Name the blood parasite species.
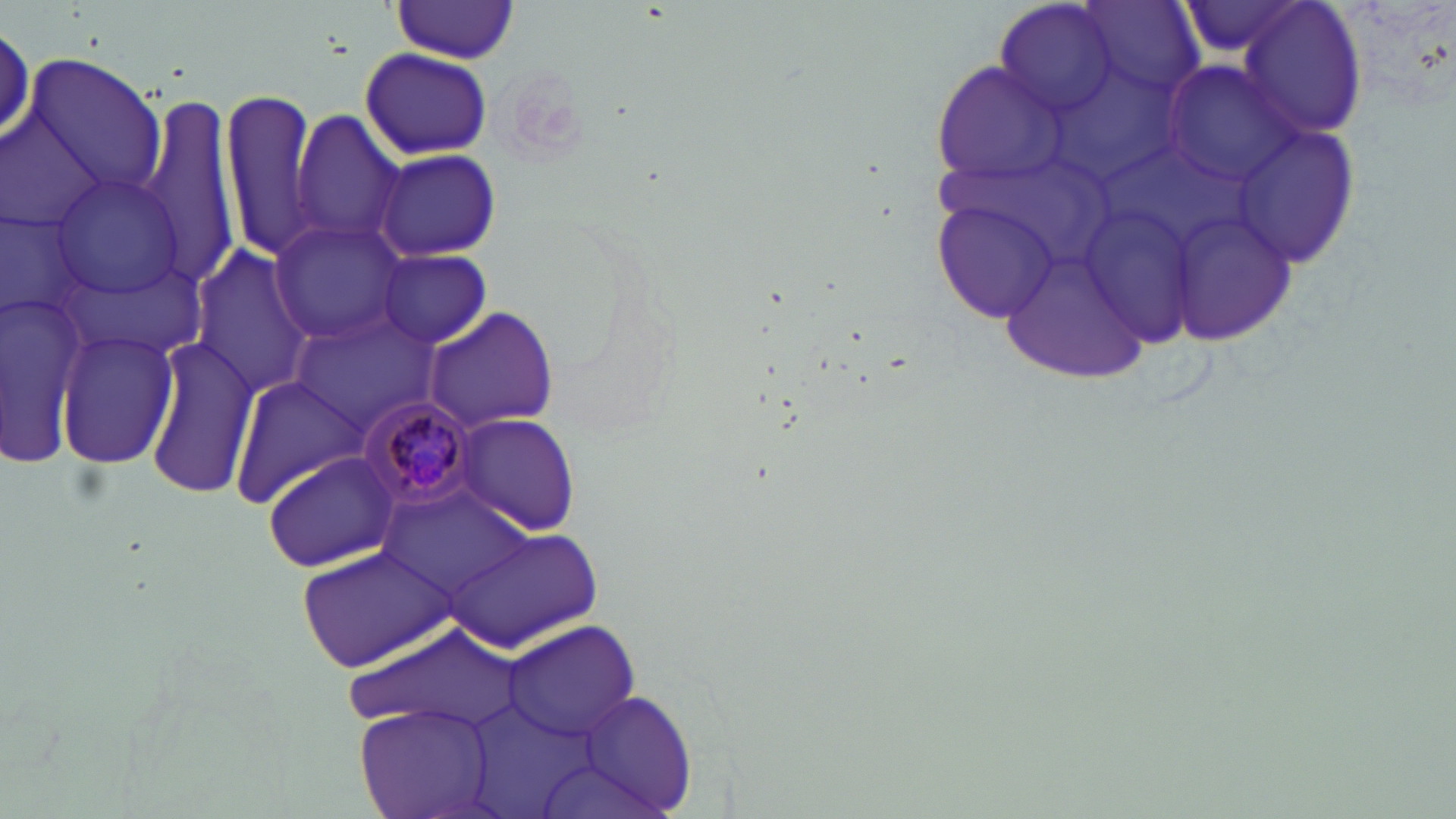

Plasmodium malariae.

Approximate bounding boxes as (x1, y1, x2, y2) in pixels. Uninfected red blood cell locations: (991, 0, 1121, 119), (1076, 1, 1203, 98), (1174, 1, 1319, 62), (387, 2, 521, 63), (1238, 2, 1367, 140), (360, 48, 492, 160), (22, 53, 165, 201), (933, 61, 1060, 188), (1160, 62, 1300, 187), (129, 90, 244, 291), (220, 90, 325, 262), (291, 109, 407, 251), (1232, 127, 1361, 268), (373, 147, 502, 261), (51, 173, 191, 298), (933, 200, 1061, 323), (1170, 206, 1302, 344), (269, 219, 409, 342), (999, 234, 1155, 388), (189, 243, 316, 399), (376, 250, 493, 347), (1, 282, 98, 465), (422, 305, 561, 431), (296, 313, 440, 424), (56, 329, 180, 471), (144, 338, 260, 499), (228, 373, 370, 508), (453, 414, 583, 535), (262, 450, 404, 573), (379, 485, 535, 605), (448, 524, 605, 651), (298, 545, 457, 671), (502, 620, 642, 744), (349, 623, 531, 734), (568, 690, 697, 812), (356, 703, 496, 819). Plasmodium malariae-infected red blood cell locations: (356, 397, 478, 516). Optical microscopy. Thin blood film. May-Grünwald-Giemsa-stained preparation. Captured at 1000x magnification. One field of a larger specimen. Image is 1456×819 pixels.